State the preparation type.
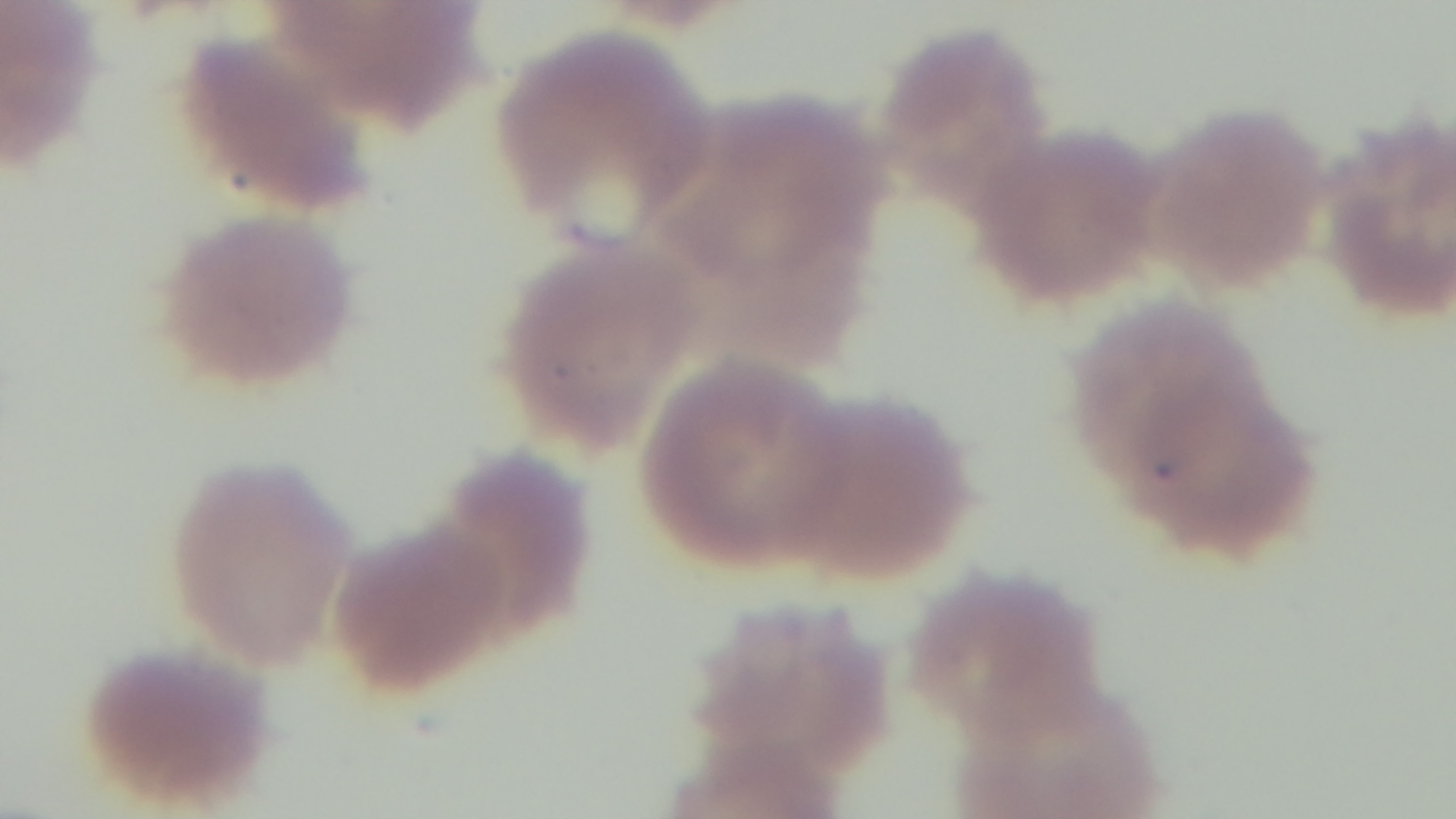
Thin.

Summary:
  - Capture: mounted 4K digital camera
  - Malaria status: positive
  - Modality: light microscopy
  - Field of view: single
  - Objective: 100x oil immersion
  - Stain: Giemsa